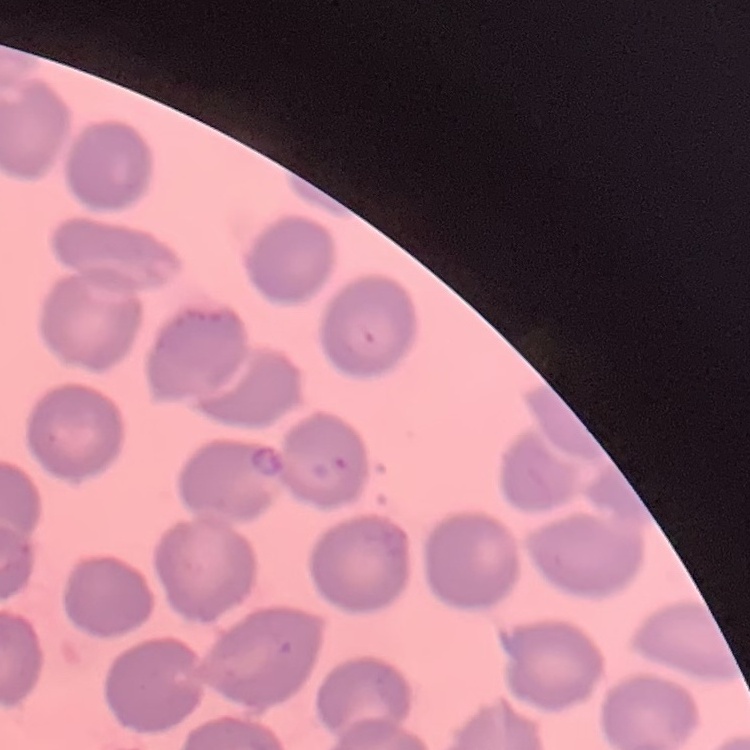

Summary:
  - Erythrocyte morphology: no rouleaux formation
  - Preparation: thin blood film
  - Image type: square crop of a larger photomicrograph
  - Stain: Field's or Giemsa